Name the blood parasite species.
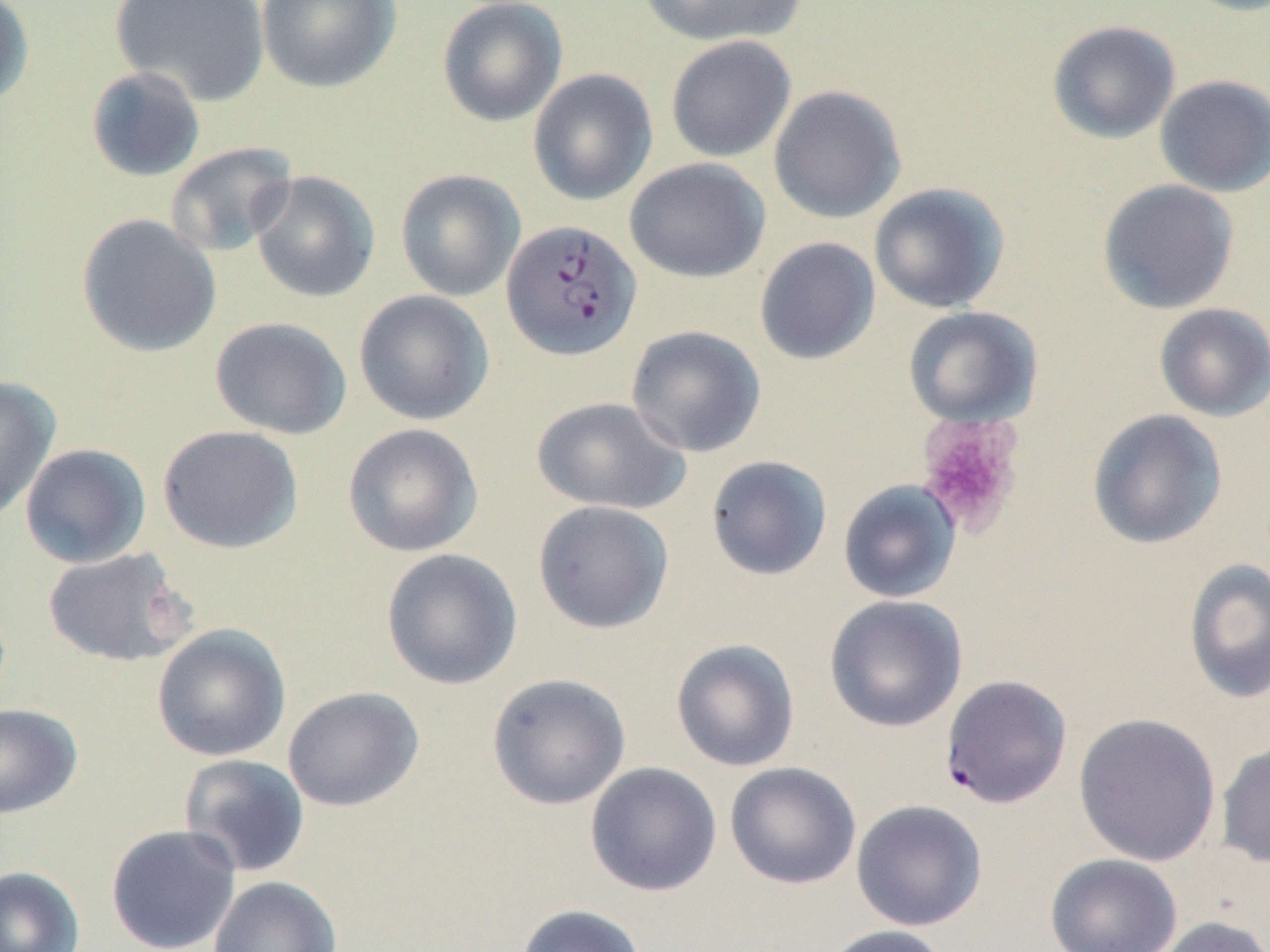
Plasmodium falciparum.

preparation: thin blood smear
plasmodium_falciparum_infected_red_blood_cell_locations: 'approximate bounding boxes as (x1, y1, x2, y2) in pixels: (500, 219, 641, 361), (940, 674, 1072, 809)'
stain: May-Grünwald-Giemsa
platelet_locations_subset: 'approximate bounding boxes as (x1, y1, x2, y2) in pixels: (915, 414, 1025, 537)'
image_size: 1270×952 pixels
field_of_view: single
modality: optical microscopy
uninfected_red_blood_cell_locations_subset: 'approximate bounding boxes as (x1, y1, x2, y2) in pixels: (0, 0, 34, 107), (110, 0, 270, 107), (256, 0, 401, 93), (437, 0, 568, 127), (635, 0, 808, 47), (1047, 20, 1181, 144), (665, 35, 797, 163), (86, 66, 206, 182), (527, 68, 658, 206), (1154, 74, 1270, 197), (768, 85, 906, 223), (164, 141, 298, 258), (624, 157, 770, 283), (395, 169, 526, 301), (250, 170, 381, 302), (1097, 179, 1239, 314), (868, 182, 1010, 314), (75, 213, 222, 358), (754, 237, 881, 365), (353, 289, 494, 425), (1153, 303, 1270, 422), (209, 316, 352, 440), (625, 324, 767, 458), (0, 375, 61, 523), (531, 396, 691, 515), (1087, 409, 1228, 550), (342, 423, 483, 557), (157, 424, 304, 554), (19, 443, 151, 569), (705, 455, 833, 581), (838, 479, 962, 604), (532, 500, 674, 634), (43, 547, 197, 667), (380, 547, 523, 690), (1183, 557, 1270, 704), (823, 595, 968, 732), (151, 623, 291, 762), (670, 638, 801, 772), (487, 673, 631, 810), (282, 686, 425, 812), (0, 703, 83, 820), (1073, 712, 1222, 866), (1216, 739, 1270, 868), (178, 753, 311, 877), (585, 761, 722, 897), (724, 761, 862, 890), (851, 799, 988, 931), (105, 824, 242, 952), (1044, 853, 1182, 952), (0, 864, 85, 952), (207, 876, 343, 952), (516, 903, 648, 952), (1150, 915, 1270, 952), (817, 924, 953, 952)'
magnification: 1000x